Report the malaria status of this cell.
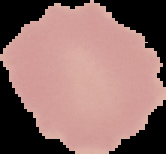

Uninfected.

Summary:
  - Image type: cell region segmented out of the field of view; surrounding area masked to black
  - Preparation: thin blood film
  - Image size: 166×154 pixels